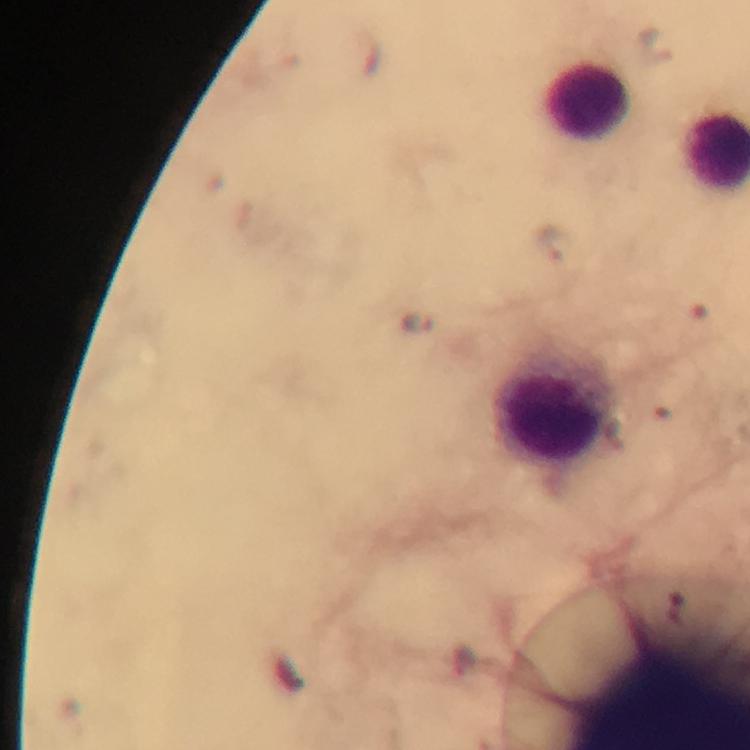
Approximate object centers, in pixels from the top-left corner. Malaria parasite locations: (x=552, y=244), (x=416, y=321). Leukocyte locations: (x=588, y=97), (x=551, y=413). At 100x magnification. Thick blood film. Photographed through the microscope with a smartphone camera. Immersion oil was used. Image is 750×750 pixels. From a diagnostic examination for malaria. Giemsa-stained preparation. A crop from one field of view.